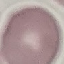

Summary:
  - Malaria status: uninfected
  - Image type: automatically extracted cell patch, resized to 64 × 64 pixels
  - Stain: Giemsa
  - Capture: smartphone through the microscope eyepiece
  - Preparation: thin smear